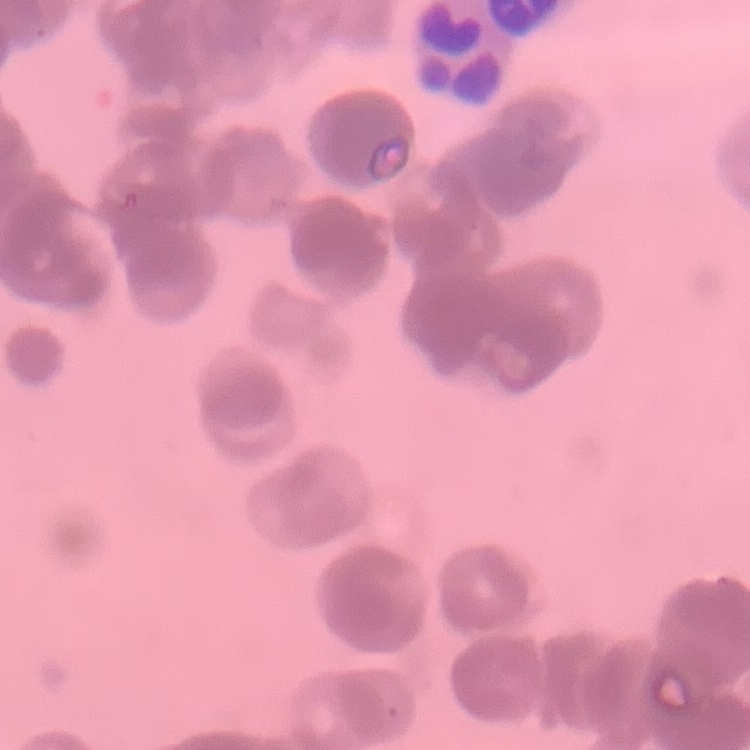

red_blood_cell_morphology: rouleaux formation
stain: Field's or Giemsa
preparation: thin blood smear
image_type: one tile cut from a larger photomicrograph